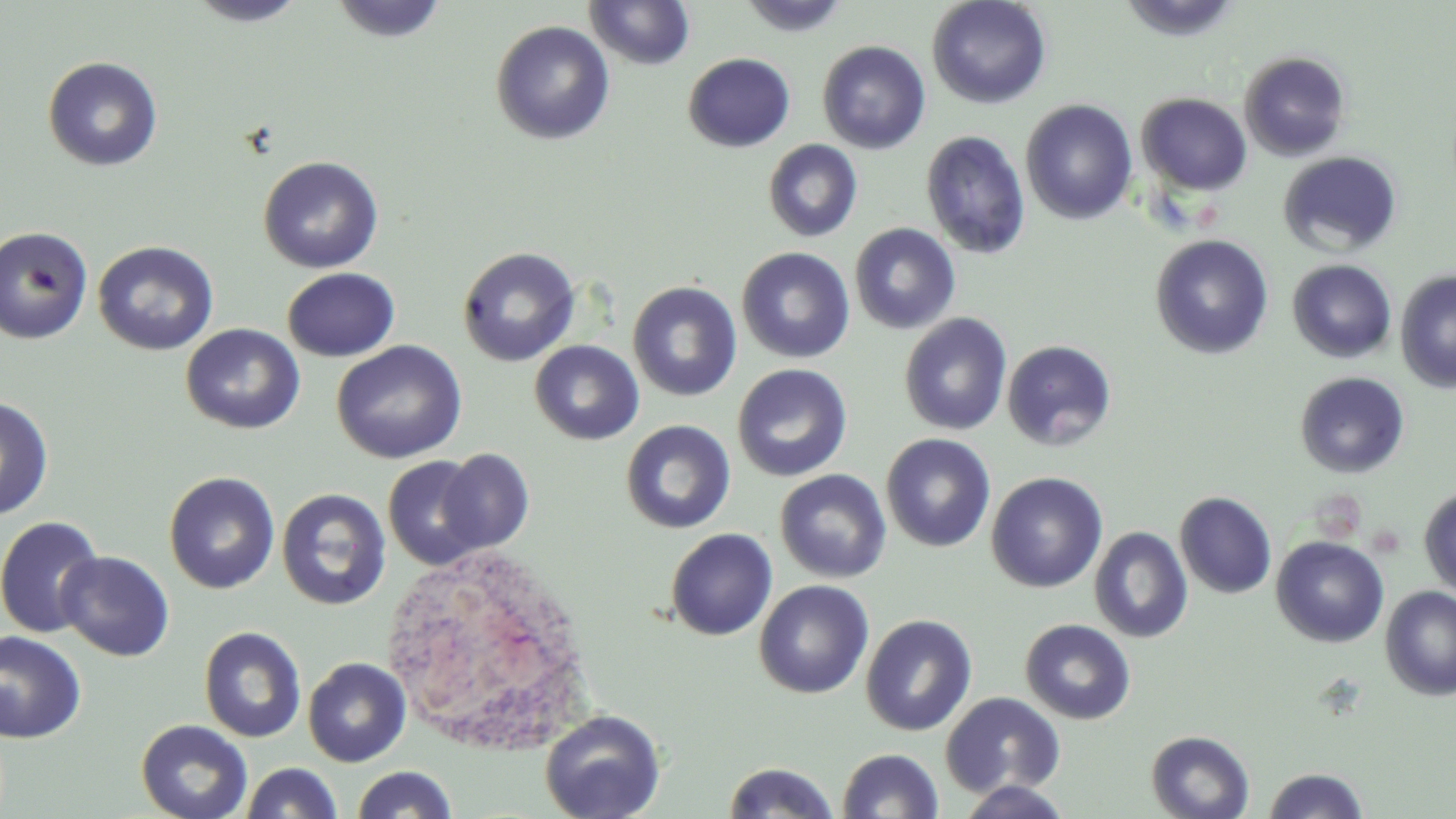

{
  "slide_level_diagnosis": "no evidence of blood parasites",
  "magnification": "1000x",
  "modality": "light microscopy",
  "white_blood_cell_locations": "approximate bounding boxes as named x1/y1/x2/y2 corners in pixels: (x1=385, y1=543, x2=602, y2=759)",
  "uninfected_red_blood_cell_locations": "approximate bounding boxes as named x1/y1/x2/y2 corners in pixels: (x1=186, y1=0, x2=310, y2=27), (x1=329, y1=0, x2=448, y2=43), (x1=738, y1=0, x2=852, y2=38), (x1=927, y1=0, x2=1052, y2=110), (x1=1116, y1=0, x2=1245, y2=42), (x1=584, y1=1, x2=696, y2=70), (x1=490, y1=20, x2=615, y2=145), (x1=817, y1=40, x2=931, y2=154), (x1=1239, y1=51, x2=1351, y2=161), (x1=682, y1=52, x2=796, y2=153), (x1=42, y1=56, x2=163, y2=171), (x1=1137, y1=93, x2=1252, y2=196), (x1=1021, y1=99, x2=1137, y2=225), (x1=920, y1=130, x2=1031, y2=259), (x1=762, y1=139, x2=863, y2=242), (x1=1278, y1=151, x2=1402, y2=258), (x1=258, y1=155, x2=384, y2=274), (x1=849, y1=223, x2=961, y2=334), (x1=0, y1=226, x2=94, y2=345), (x1=1150, y1=234, x2=1273, y2=359), (x1=92, y1=240, x2=219, y2=356), (x1=457, y1=246, x2=581, y2=367), (x1=736, y1=247, x2=855, y2=363), (x1=1287, y1=259, x2=1397, y2=363), (x1=282, y1=268, x2=400, y2=362), (x1=1395, y1=269, x2=1456, y2=394), (x1=627, y1=280, x2=742, y2=401), (x1=898, y1=313, x2=1012, y2=435), (x1=180, y1=323, x2=305, y2=434), (x1=331, y1=340, x2=468, y2=464), (x1=529, y1=340, x2=645, y2=445), (x1=1001, y1=340, x2=1117, y2=451), (x1=732, y1=364, x2=852, y2=481), (x1=1295, y1=371, x2=1410, y2=478), (x1=0, y1=395, x2=54, y2=520), (x1=620, y1=419, x2=736, y2=534), (x1=881, y1=433, x2=995, y2=552), (x1=437, y1=448, x2=535, y2=555), (x1=383, y1=455, x2=490, y2=570), (x1=775, y1=469, x2=892, y2=582), (x1=164, y1=471, x2=281, y2=594), (x1=986, y1=472, x2=1108, y2=592), (x1=1418, y1=486, x2=1456, y2=600), (x1=276, y1=488, x2=391, y2=611), (x1=1175, y1=492, x2=1277, y2=599), (x1=0, y1=515, x2=105, y2=639), (x1=1089, y1=526, x2=1192, y2=644), (x1=665, y1=528, x2=777, y2=641), (x1=1271, y1=535, x2=1390, y2=648), (x1=55, y1=551, x2=174, y2=661), (x1=753, y1=580, x2=873, y2=699), (x1=1380, y1=586, x2=1456, y2=700), (x1=860, y1=614, x2=978, y2=737), (x1=1020, y1=618, x2=1136, y2=724), (x1=199, y1=626, x2=306, y2=743), (x1=0, y1=630, x2=87, y2=744), (x1=303, y1=657, x2=411, y2=767), (x1=940, y1=691, x2=1065, y2=798), (x1=539, y1=709, x2=665, y2=819), (x1=136, y1=719, x2=253, y2=819), (x1=1146, y1=729, x2=1255, y2=819), (x1=837, y1=748, x2=944, y2=818), (x1=722, y1=761, x2=840, y2=819), (x1=240, y1=762, x2=344, y2=819), (x1=351, y1=765, x2=458, y2=819), (x1=1263, y1=767, x2=1368, y2=819), (x1=955, y1=780, x2=1074, y2=818)",
  "preparation": "thin blood film",
  "stain": "May-Grünwald-Giemsa",
  "image_size": "1456×819 pixels",
  "field_of_view": "one of a larger specimen"
}